Locate every blood parasite and identify its species.
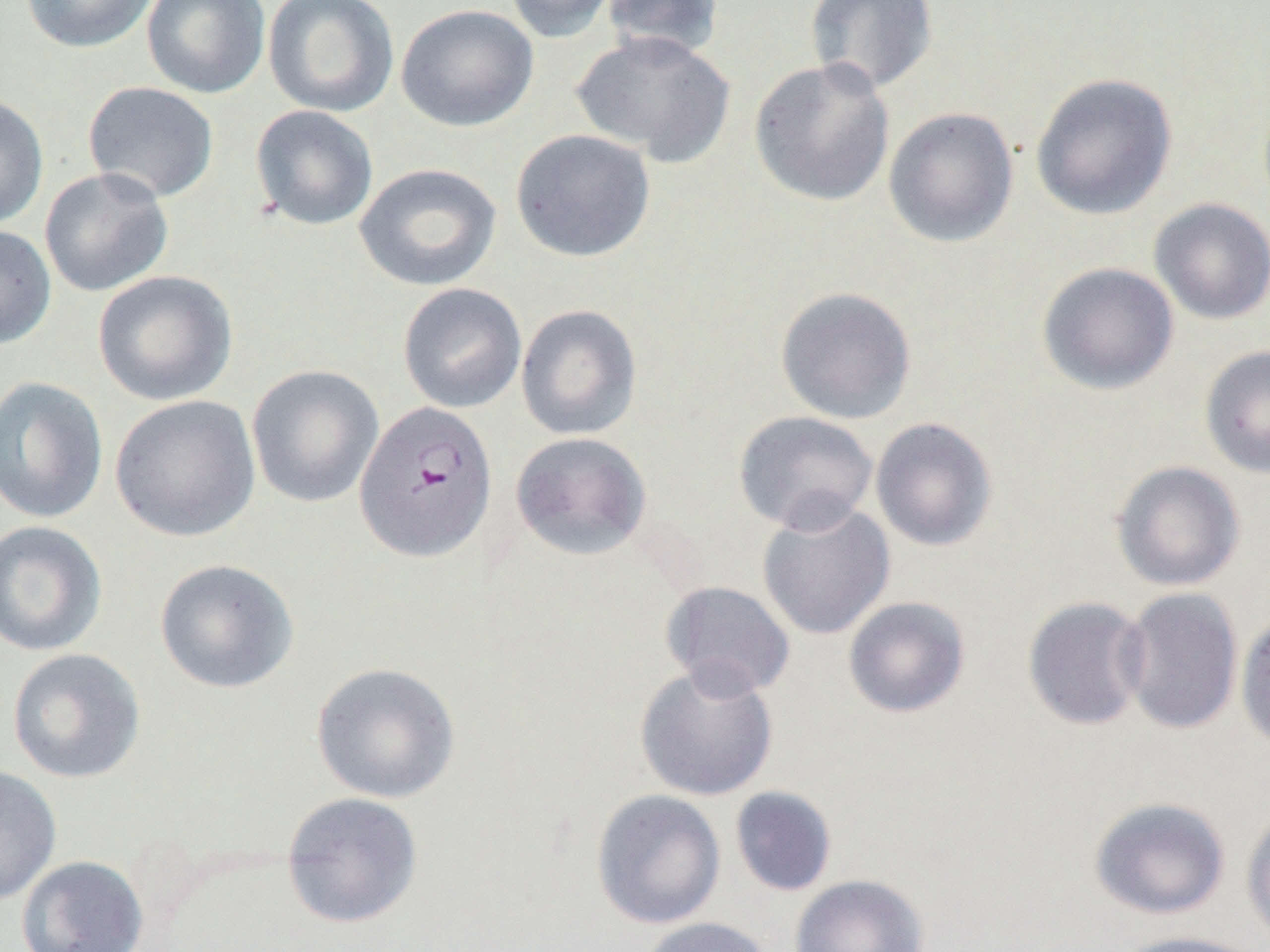

Approximate bounding boxes as (x1,y1)-(x2,y2) corner pairs in pixels.
Plasmodium falciparum-infected red blood cells: (353,399)-(498,564).
No Plasmodium ovale, Plasmodium malariae, Plasmodium vivax, Babesia divergens, or Trypanosoma brucei observed.

slide-level diagnosis = Plasmodium falciparum
uninfected red blood cell locations = approximate bounding boxes as (x1,y1)-(x2,y2) corner pairs in pixels: (21,0)-(158,53), (142,0)-(270,99), (262,0)-(399,118), (503,0)-(621,44), (600,0)-(725,63), (804,0)-(940,95), (395,3)-(539,132), (570,31)-(735,168), (749,57)-(895,207), (1030,72)-(1178,220), (82,81)-(219,204), (0,92)-(49,231), (249,104)-(379,231), (883,106)-(1019,248), (510,129)-(656,263), (354,162)-(502,291), (39,167)-(174,298), (1148,197)-(1270,325), (0,224)-(57,350), (1036,262)-(1179,395), (92,269)-(238,406), (397,282)-(527,413), (774,286)-(917,424), (515,304)-(642,441), (1200,344)-(1270,480), (246,364)-(384,508), (0,375)-(109,524), (110,394)-(261,542), (732,410)-(879,534), (870,417)-(998,552), (510,431)-(652,561), (1111,460)-(1245,592), (756,500)-(896,641), (0,520)-(108,657), (154,558)-(299,694), (659,581)-(795,699), (1117,587)-(1244,735), (1022,595)-(1152,731), (842,596)-(971,719), (1234,609)-(1270,752), (6,647)-(147,784), (634,660)-(780,802), (311,662)-(461,804), (0,764)-(62,905), (729,786)-(837,897), (591,789)-(726,929), (281,791)-(424,928), (1089,797)-(1230,920), (1241,806)-(1270,946), (17,854)-(149,951), (789,874)-(930,952), (636,916)-(775,952), (1112,930)-(1264,952)
field of view = one of a larger specimen
magnification = 1000x
modality = optical microscopy
image size = 1270×952 pixels
preparation = thin blood smear